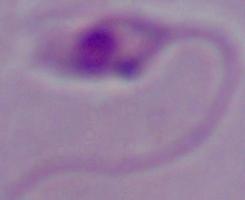
1000x magnification. A Leishmania parasite is shown. Photomicrograph.